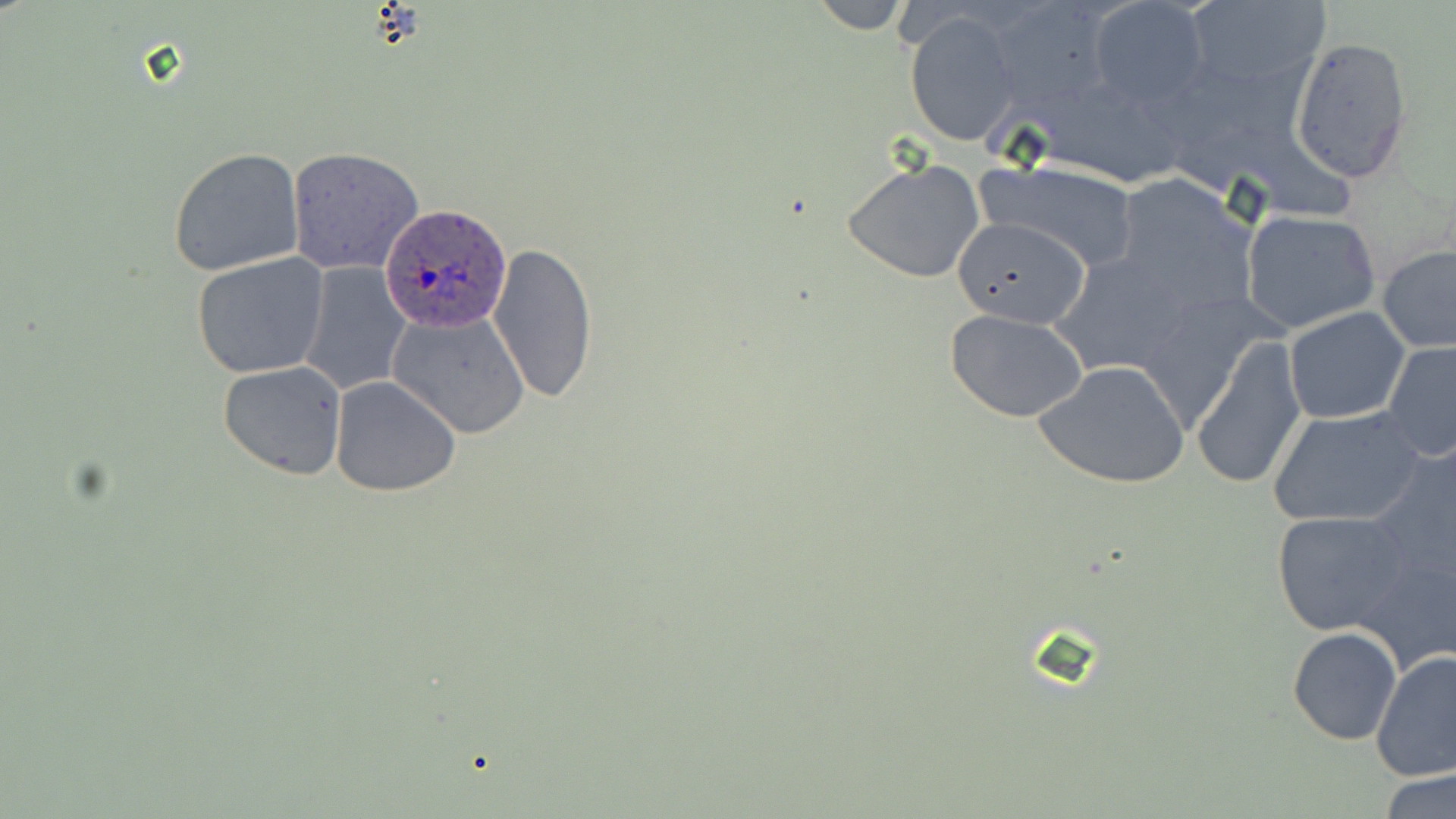
Approximate bounding boxes as [x1, y1, x2, y2] in pixels. Uninfected red blood cell locations: [807, 0, 915, 32], [1085, 0, 1209, 110], [1180, 1, 1330, 96], [906, 11, 1020, 147], [1288, 35, 1415, 184], [168, 147, 305, 276], [285, 147, 423, 276], [977, 157, 1141, 272], [842, 158, 987, 285], [1114, 174, 1259, 318], [1240, 209, 1384, 336], [954, 214, 1092, 326], [486, 242, 600, 404], [1377, 245, 1456, 354], [1050, 249, 1195, 377], [192, 252, 330, 378], [299, 261, 412, 397], [1132, 284, 1280, 441], [1283, 306, 1411, 425], [944, 308, 1092, 423], [387, 309, 530, 438], [1191, 334, 1306, 492], [334, 336, 513, 470], [1382, 340, 1456, 461], [218, 360, 347, 481], [1034, 360, 1190, 489], [329, 376, 461, 497], [1268, 405, 1426, 528], [1366, 437, 1456, 596], [1270, 509, 1415, 636], [1352, 544, 1456, 675], [1287, 626, 1402, 745], [1371, 649, 1456, 781], [1379, 769, 1456, 819]. Plasmodium ovale-infected red blood cell locations: [380, 205, 511, 331]. Slide-level diagnosis: Plasmodium ovale. Optical microscopy. Thin blood smear. Captured at 1000x magnification. Image is 1456×819 pixels. One field of a larger specimen. May-Grünwald-Giemsa stain.